Locate every Plasmodium parasite and identify its life-cycle stage.
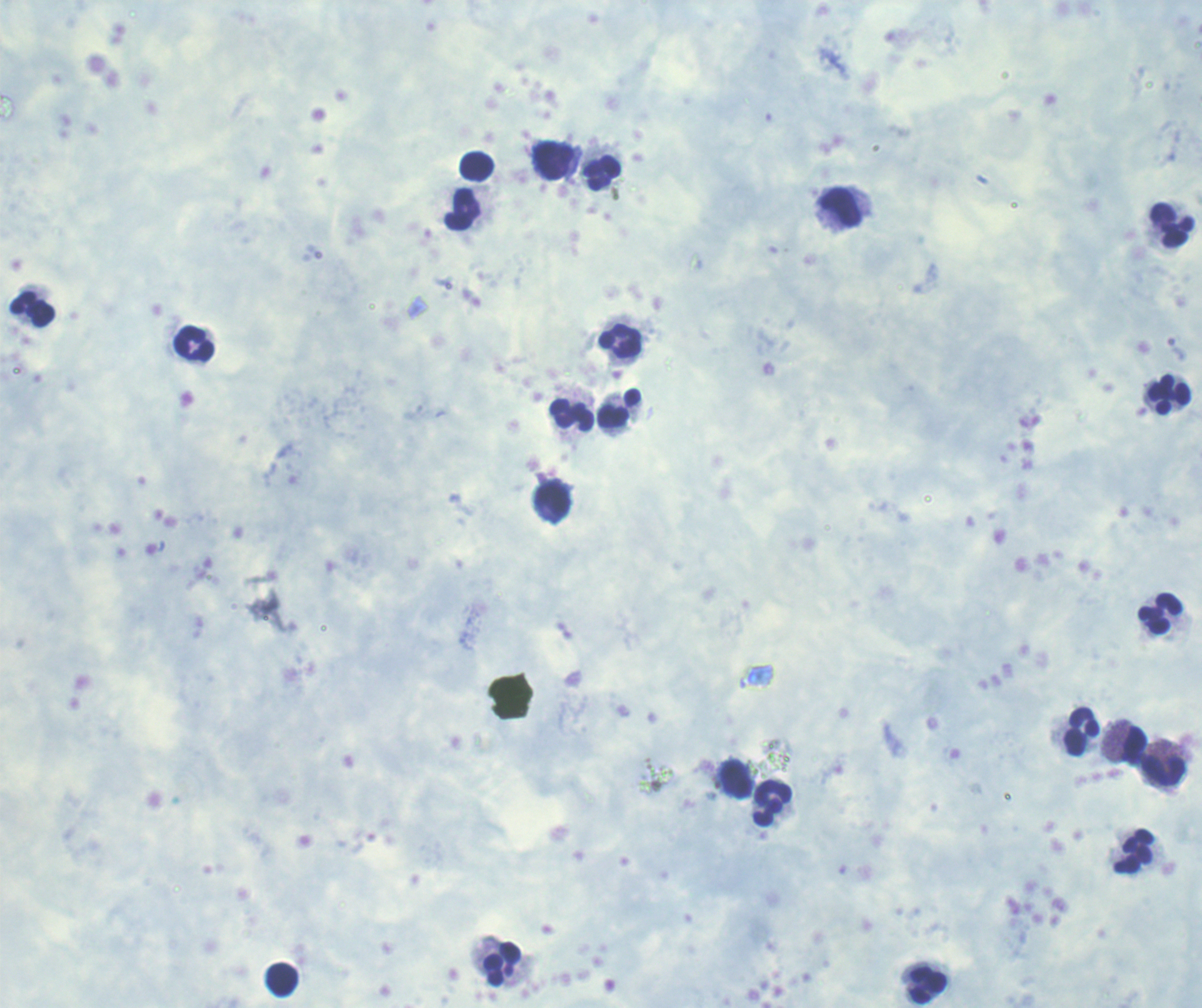
No Plasmodium parasites detected.

coordinate format = approximate centers as (x, y) in pixels
leukocyte locations = (554, 161), (477, 166), (602, 173), (841, 208), (462, 210), (1173, 226), (32, 309), (621, 340), (194, 345), (1168, 395), (619, 408), (573, 416), (552, 498), (1159, 613), (1082, 732), (1135, 744), (1163, 771), (738, 779), (773, 803), (1134, 852), (504, 965), (284, 980), (928, 987)
preparation = thick blood smear
magnification = 100x
stain = Romanowsky
field of view = single
context = previously used in a real diagnosis
image size = 1202×1008 pixels
background quality = unsatisfactory